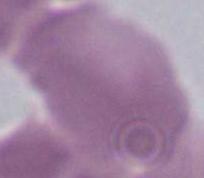

Captured at 1000x magnification. An erythrocyte is seen. Photomicrograph.